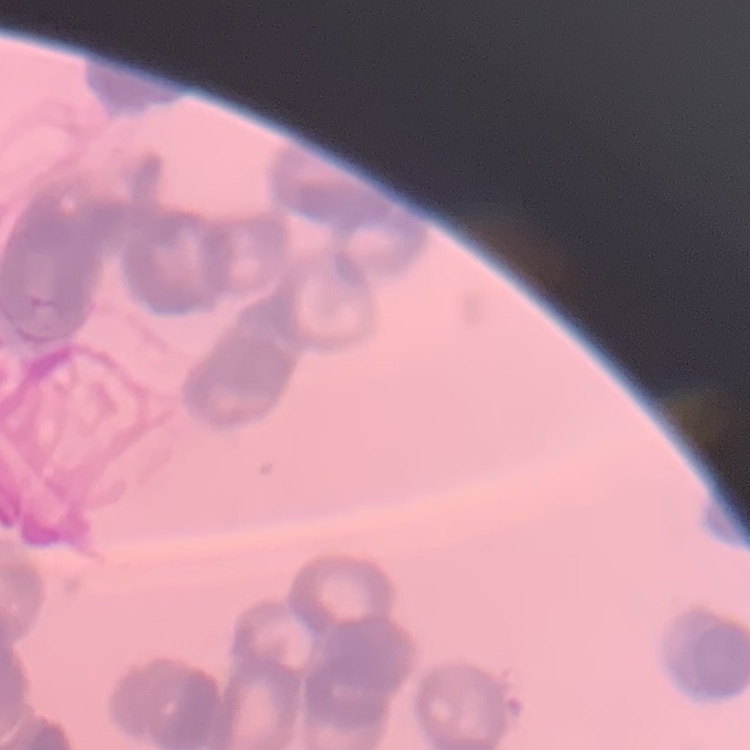
The red blood cells exhibit rouleaux formation. One tile cut from a larger photomicrograph. Thin blood smear. Stained with either Field's or Giemsa.